Give the position of every Plasmodium parasite.
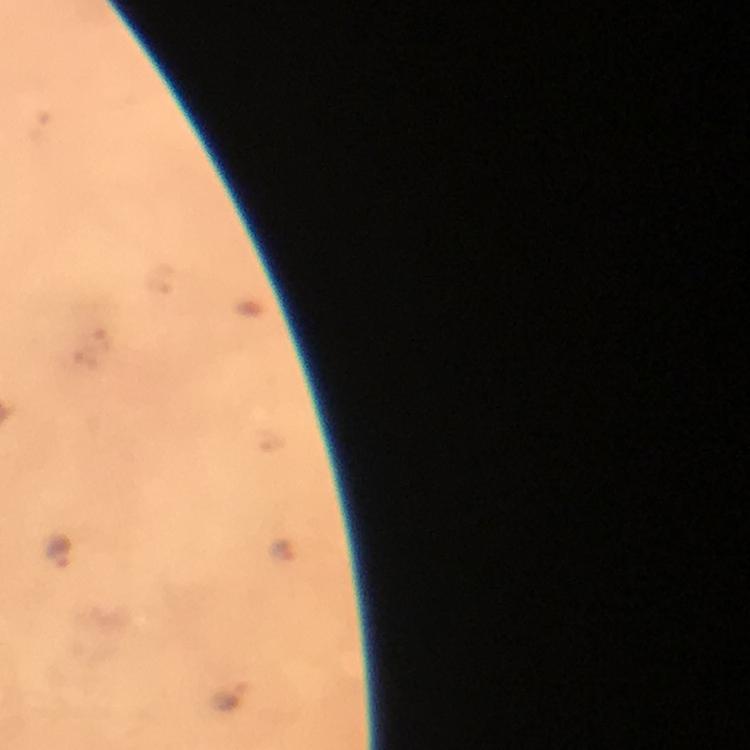
Approximate object centers, in pixels from the top-left corner.
Plasmodium parasites: (x=282, y=551), (x=60, y=552), (x=232, y=697).

context = from a diagnostic examination for malaria
capture = smartphone mounted on the microscope
image size = 750×750 pixels
stain = Giemsa
preparation = thick blood smear
cropped from = one field of view
immersion oil = applied
magnification = 100x